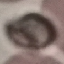

malaria_status: uninfected
capture: smartphone camera at the microscope eyepiece
stain: Giemsa
image_type: cell patch, automatically extracted from a larger field of view and resized to 64 × 64 pixels
preparation: thin smear